Outline platelets.
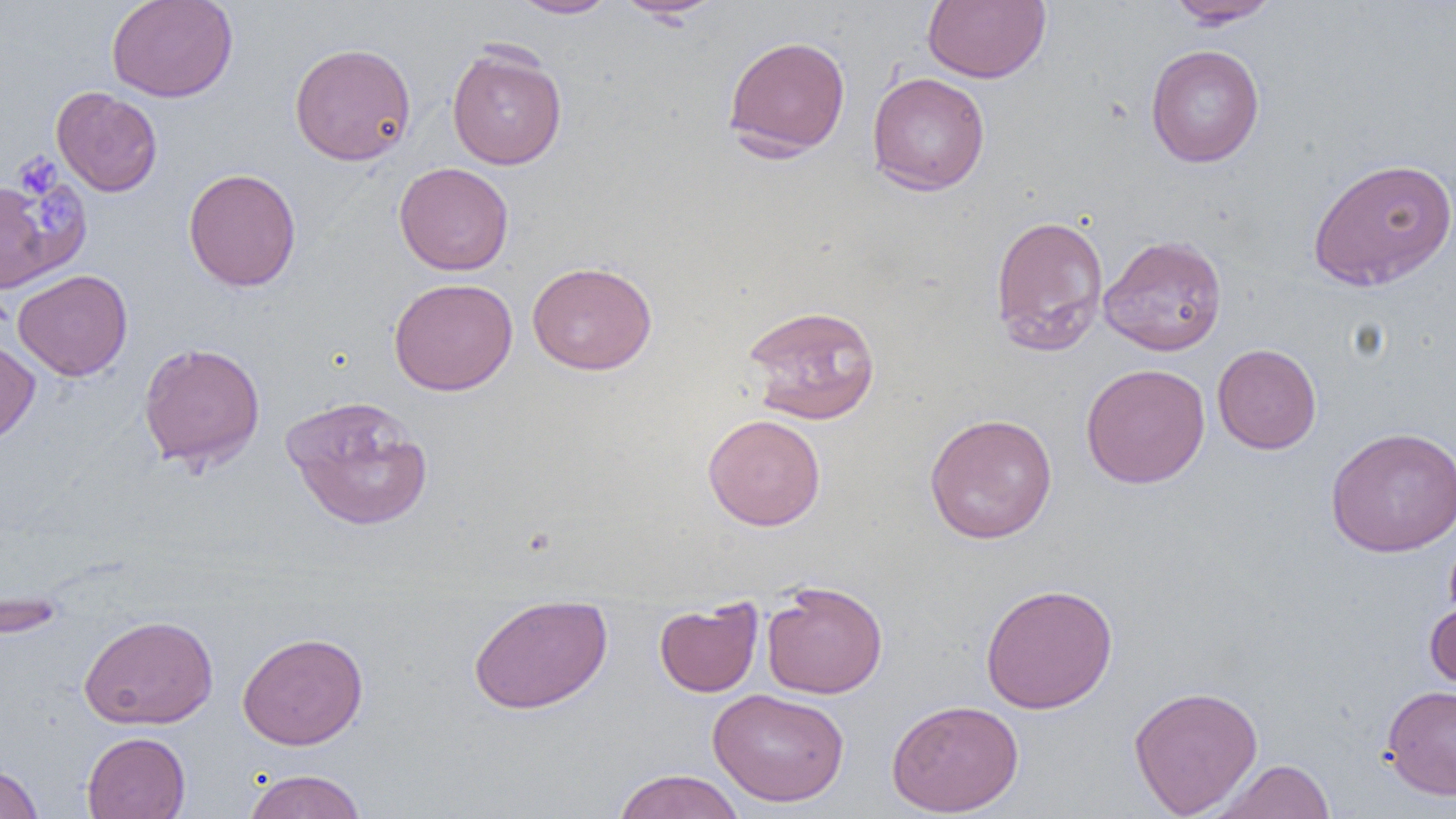
Approximate bounding boxes as (x1,y1)-(x2,y2) corner pairs in pixels.
Platelets: (15,153)-(61,199), (31,189)-(80,232).

slide-level diagnosis = negative for blood parasites
magnification = 1000x
uninfected red blood cell locations = approximate bounding boxes as (x1,y1)-(x2,y2) corner pairs in pixels: (106,0)-(238,102), (509,0)-(619,19), (614,0)-(726,22), (923,0)-(1051,83), (1166,0)-(1281,28), (722,35)-(852,160), (289,41)-(417,166), (1146,44)-(1264,168), (447,45)-(567,170), (866,71)-(991,196), (51,86)-(163,197), (1307,156)-(1456,291), (394,162)-(514,276), (183,167)-(301,291), (0,179)-(79,292), (989,214)-(1109,356), (1098,234)-(1228,356), (527,261)-(657,375), (12,269)-(133,381), (389,277)-(518,396), (742,303)-(881,424), (0,339)-(40,447), (138,341)-(266,471), (1212,343)-(1322,454), (1081,363)-(1210,489), (280,394)-(433,530), (702,413)-(826,531), (924,413)-(1057,544), (1325,426)-(1456,557), (761,580)-(888,698), (980,583)-(1118,714), (468,594)-(612,714), (1424,595)-(1456,697), (654,599)-(763,697), (79,614)-(219,730), (237,631)-(368,750), (1128,684)-(1264,817), (1381,684)-(1456,800), (707,688)-(850,807), (886,698)-(1024,817), (82,731)-(191,819), (1209,759)-(1336,818), (0,763)-(44,819), (241,768)-(368,819), (611,768)-(745,819)
field of view = one of a larger specimen
modality = optical microscopy
preparation = thin blood film
image size = 1456×819 pixels